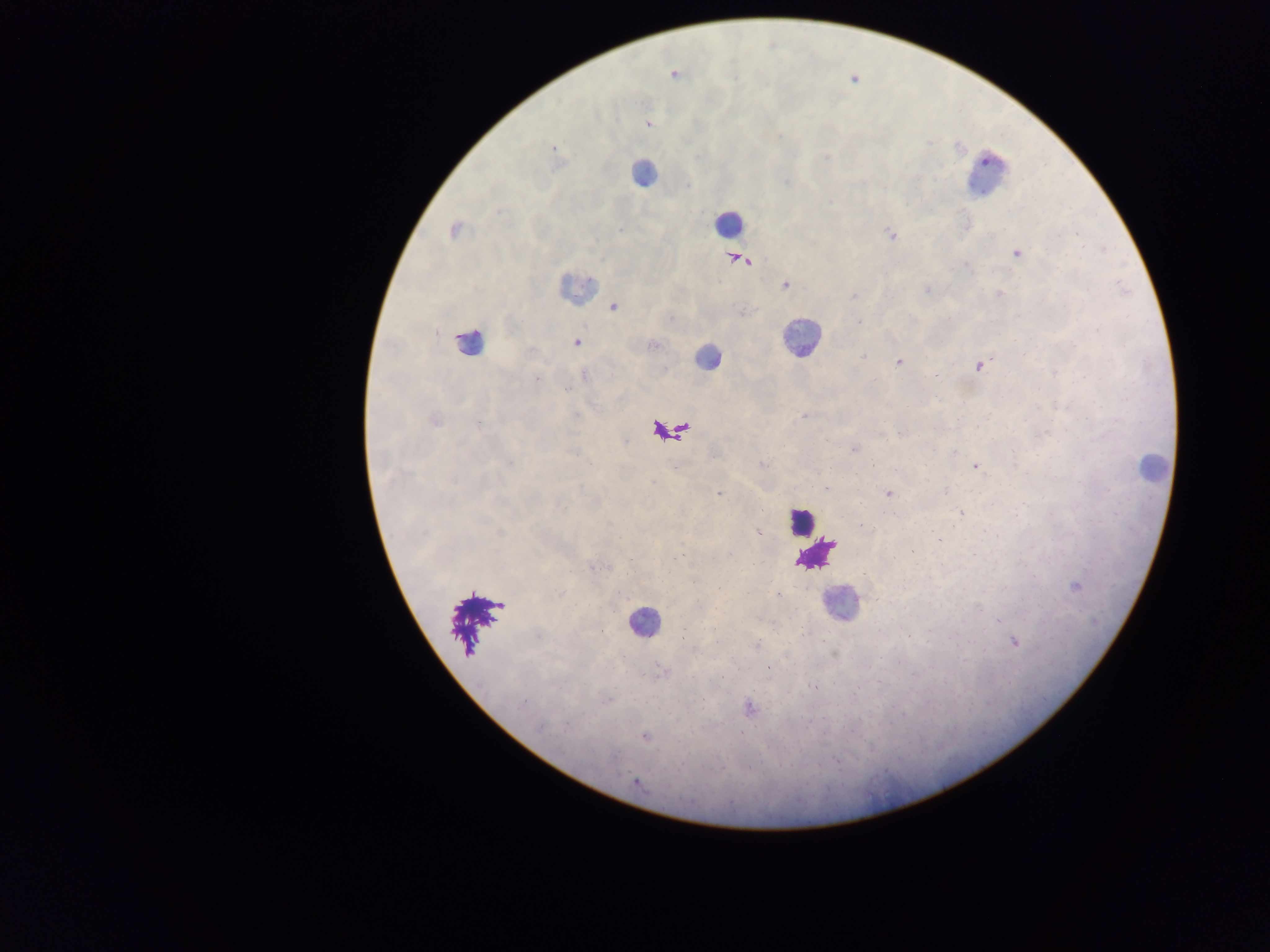

Approximate centers as (x, y) in pixels. Leukocyte locations: (643, 173), (984, 176), (727, 223), (575, 289), (801, 338), (470, 341), (707, 358), (1152, 469), (802, 520), (816, 555), (841, 605), (643, 622). Plasmodium parasite locations: (673, 74), (853, 79), (647, 123), (553, 147), (454, 231), (892, 234), (1016, 254), (736, 260), (784, 284), (926, 290), (999, 294), (614, 307), (577, 342), (898, 361), (978, 366), (935, 375), (535, 377), (804, 417), (434, 420), (901, 432), (854, 449), (975, 466), (719, 493), (888, 493), (961, 513), (758, 534), (1075, 586), (778, 595), (1014, 641), (768, 668), (814, 687), (749, 708), (645, 737), (635, 781). Collected in Ghana. Mobile-phone photograph taken through the microscope. Image is 1270×952 pixels. Thick blood smear. Single field of view.